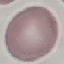

result = no malaria parasites detected
capture = smartphone through the microscope eyepiece
image type = automatically extracted cell patch, resized to 64 × 64 pixels
stain = Giemsa
preparation = thin blood smear